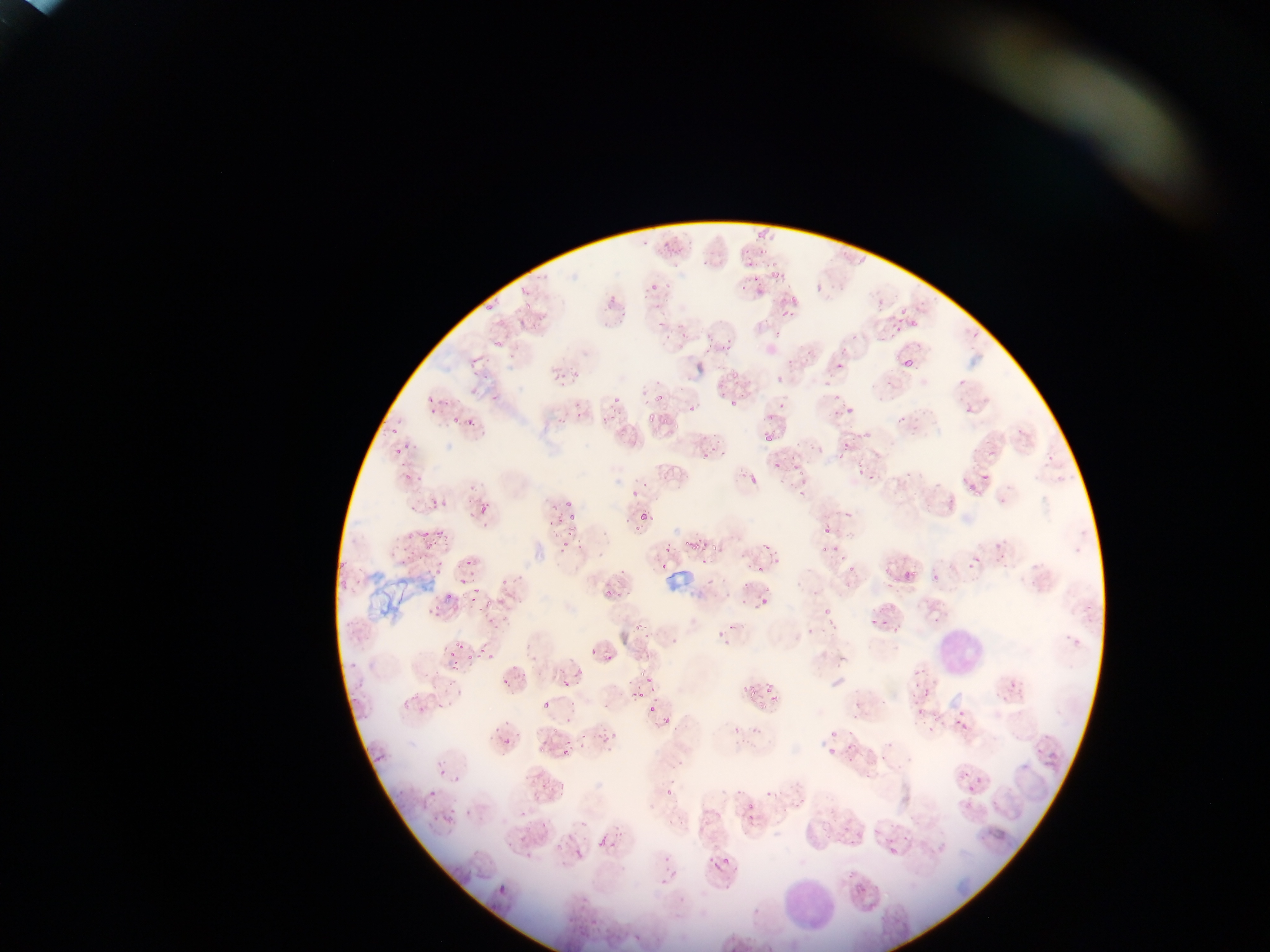
image size = 1270×952 pixels
capture = mobile-phone photograph through a microscope
field of view = single
country = Ghana
leukocyte locations = approximate bounding boxes as {left, top, right, bottom} in pixels: {933, 626, 986, 680}, {777, 877, 836, 935}
Plasmodium parasite locations = approximate bounding boxes as {left, top, right, bottom} in pixels (subset; some below the resolvable size): {753, 232, 763, 241}, {641, 238, 652, 247}, {660, 238, 671, 247}, {744, 246, 751, 256}, {665, 248, 677, 258}, {758, 248, 766, 256}, {745, 259, 754, 269}, {701, 260, 710, 268}, {672, 263, 681, 270}, {768, 270, 777, 279}, {780, 272, 787, 281}, {649, 279, 658, 291}, {739, 282, 749, 292}, {789, 293, 795, 306}, {605, 294, 618, 304}, {875, 299, 884, 314}, {485, 301, 495, 312}, {654, 302, 664, 310}, {522, 305, 530, 311}, {897, 308, 905, 315}, {780, 310, 788, 318}, {895, 314, 904, 325}, {536, 316, 546, 320}, {516, 317, 527, 327}, {491, 318, 504, 327}, {657, 319, 667, 327}, {888, 322, 902, 333}, {910, 322, 920, 330}, {705, 331, 713, 344}, {774, 331, 782, 336}, {966, 331, 977, 341}, {681, 332, 689, 341}, {720, 340, 731, 350}, {495, 341, 502, 350}, {840, 343, 850, 354}, {804, 348, 814, 360}, {703, 353, 712, 359}, {470, 354, 479, 366}, {787, 360, 795, 366}, {836, 361, 845, 367}, {900, 362, 911, 369}, {731, 364, 741, 378}, {470, 369, 480, 378}, {482, 373, 491, 383}, {550, 373, 562, 381}, {568, 375, 579, 381}, {825, 375, 831, 385}, {959, 381, 967, 387}, {716, 382, 727, 389}, {560, 383, 569, 389}, {640, 383, 646, 394}, {728, 393, 742, 407}, {489, 394, 501, 402}, {654, 397, 662, 403}, {444, 398, 454, 406}, {609, 399, 620, 403}, {641, 399, 651, 407}, {777, 402, 786, 408}, {686, 403, 696, 413}, {847, 406, 853, 415}, {573, 409, 583, 417}, {600, 410, 617, 421}, {833, 410, 840, 418}, {450, 413, 457, 425}, {465, 415, 474, 426}, {647, 415, 656, 423}, {661, 415, 668, 425}, {892, 415, 905, 426}, {555, 416, 566, 424}, {671, 422, 679, 429}, {388, 429, 399, 438}, {763, 429, 770, 446}, {860, 432, 870, 442}, {714, 438, 720, 448}, {841, 442, 849, 450}, {393, 447, 402, 456}, {815, 447, 823, 453}, {701, 452, 709, 461}, {857, 459, 863, 469}, {399, 460, 408, 473}, {773, 462, 779, 470}, {793, 463, 804, 471}, {856, 467, 864, 478}, {748, 470, 758, 485}, {404, 473, 412, 480}, {868, 473, 876, 481}, {980, 475, 988, 483}, {417, 477, 425, 485}, {787, 481, 796, 487}, {466, 487, 477, 493}, {965, 487, 973, 494}, {630, 491, 639, 500}, {798, 491, 806, 499}, {405, 500, 417, 511}, {477, 500, 483, 515}, {429, 501, 437, 508}, {483, 501, 491, 513}, {566, 501, 574, 510}, {549, 505, 558, 515}, {844, 509, 855, 521}, {640, 512, 652, 524}, {568, 513, 580, 523}, {557, 516, 565, 529}, {434, 527, 449, 538}, {822, 527, 829, 535}, {421, 529, 429, 538}, {563, 530, 572, 538}, {562, 538, 572, 550}, {579, 539, 586, 549}, {684, 541, 696, 550}, {707, 542, 721, 555}, {762, 542, 769, 551}, {663, 544, 674, 552}, {832, 544, 840, 555}, {401, 546, 412, 552}, {424, 546, 432, 554}, {819, 547, 827, 553}, {1001, 552, 1009, 559}, {974, 553, 982, 564}, {700, 555, 710, 564}, {438, 556, 442, 568}, {400, 558, 408, 566}, {773, 558, 781, 564}, {468, 560, 474, 568}, {336, 561, 348, 568}, {969, 561, 973, 569}, {659, 562, 667, 570}, {1001, 563, 1009, 569}, {846, 565, 854, 571}, {757, 566, 765, 572}, {434, 567, 442, 574}, {905, 569, 922, 578}, {500, 574, 507, 585}, {706, 575, 716, 588}, {459, 576, 468, 584}, {932, 576, 940, 582}, {355, 577, 362, 585}, {339, 578, 346, 588}, {473, 585, 480, 593}, {601, 589, 612, 604}, {612, 590, 622, 601}, {445, 595, 454, 602}, {469, 595, 478, 603}, {758, 596, 771, 609}, {740, 597, 750, 610}, {433, 602, 439, 611}, {823, 607, 832, 617}, {488, 615, 497, 624}, {870, 616, 878, 626}, {883, 617, 888, 627}, {492, 621, 501, 632}, {893, 621, 904, 635}, {730, 622, 736, 631}, {632, 623, 643, 634}, {645, 631, 651, 640}, {672, 631, 683, 643}, {452, 637, 459, 645}, {459, 644, 465, 652}, {476, 645, 485, 653}, {446, 650, 455, 659}, {487, 652, 496, 663}, {603, 653, 613, 663}, {465, 654, 473, 659}, {450, 662, 461, 671}, {350, 663, 360, 668}, {577, 667, 586, 677}, {521, 669, 530, 677}, {914, 670, 928, 675}, {500, 673, 510, 683}, {645, 675, 657, 683}, {560, 676, 572, 687}, {446, 679, 455, 685}, {1006, 680, 1017, 692}, {763, 682, 774, 693}, {744, 687, 757, 698}, {922, 690, 928, 698}, {636, 692, 644, 698}, {767, 694, 783, 705}, {351, 695, 361, 702}, {567, 697, 575, 708}, {400, 699, 413, 710}, {437, 701, 449, 709}, {541, 703, 549, 712}, {757, 703, 766, 711}, {853, 703, 863, 709}, {419, 705, 429, 712}, {648, 705, 656, 713}, {958, 709, 966, 717}, {360, 714, 368, 720}, {566, 714, 577, 723}, {952, 718, 960, 726}, {960, 722, 968, 733}, {594, 725, 606, 738}, {603, 733, 614, 745}, {580, 734, 588, 740}, {503, 736, 515, 748}, {565, 737, 573, 745}, {364, 745, 372, 754}, {846, 745, 855, 751}, {538, 746, 549, 755}, {562, 747, 570, 757}, {827, 747, 836, 760}, {438, 768, 446, 777}, {963, 773, 972, 781}, {453, 775, 459, 785}, {863, 775, 872, 781}, {975, 778, 984, 786}, {541, 780, 553, 788}, {558, 782, 569, 791}, {966, 785, 974, 793}, {428, 786, 439, 797}, {747, 797, 754, 809}, {464, 807, 473, 816}, {449, 808, 457, 815}, {432, 814, 442, 824}, {667, 818, 675, 824}, {519, 833, 530, 844}, {598, 838, 608, 848}, {506, 839, 515, 847}, {577, 848, 585, 856}, {886, 848, 900, 855}, {665, 853, 672, 862}, {722, 856, 730, 865}, {663, 865, 672, 872}, {499, 882, 507, 894} | approximate {x, y} pixel centers of objects too small to bound: {758, 278}, {669, 285}, {520, 292}, {644, 298}, {792, 315}, {668, 336}, {854, 336}, {890, 383}, {836, 397}, {430, 399}, {433, 411}, {968, 411}, {407, 447}, {415, 447}, {713, 449}, {839, 458}, {801, 473}, {951, 499}, {442, 505}, {410, 534}, {419, 554}, {427, 572}, {746, 584}, {489, 603}, {481, 610}, {720, 633}, {593, 652}, {918, 686}, {653, 688}, {433, 689}, {914, 698}, {656, 700}, {919, 714}, {856, 717}, {666, 722}, {834, 736}, {884, 760}, {851, 762}, {666, 794}, {523, 815}, {543, 825}, {529, 858}, {675, 872}
preparation = thin blood smear